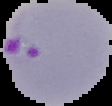

Summary:
  - Image size: 112×106 pixels
  - Malaria status: parasitized
  - Image type: segmented cell region on a black background
  - Preparation: thin blood smear